Look for Plasmodium parasites.
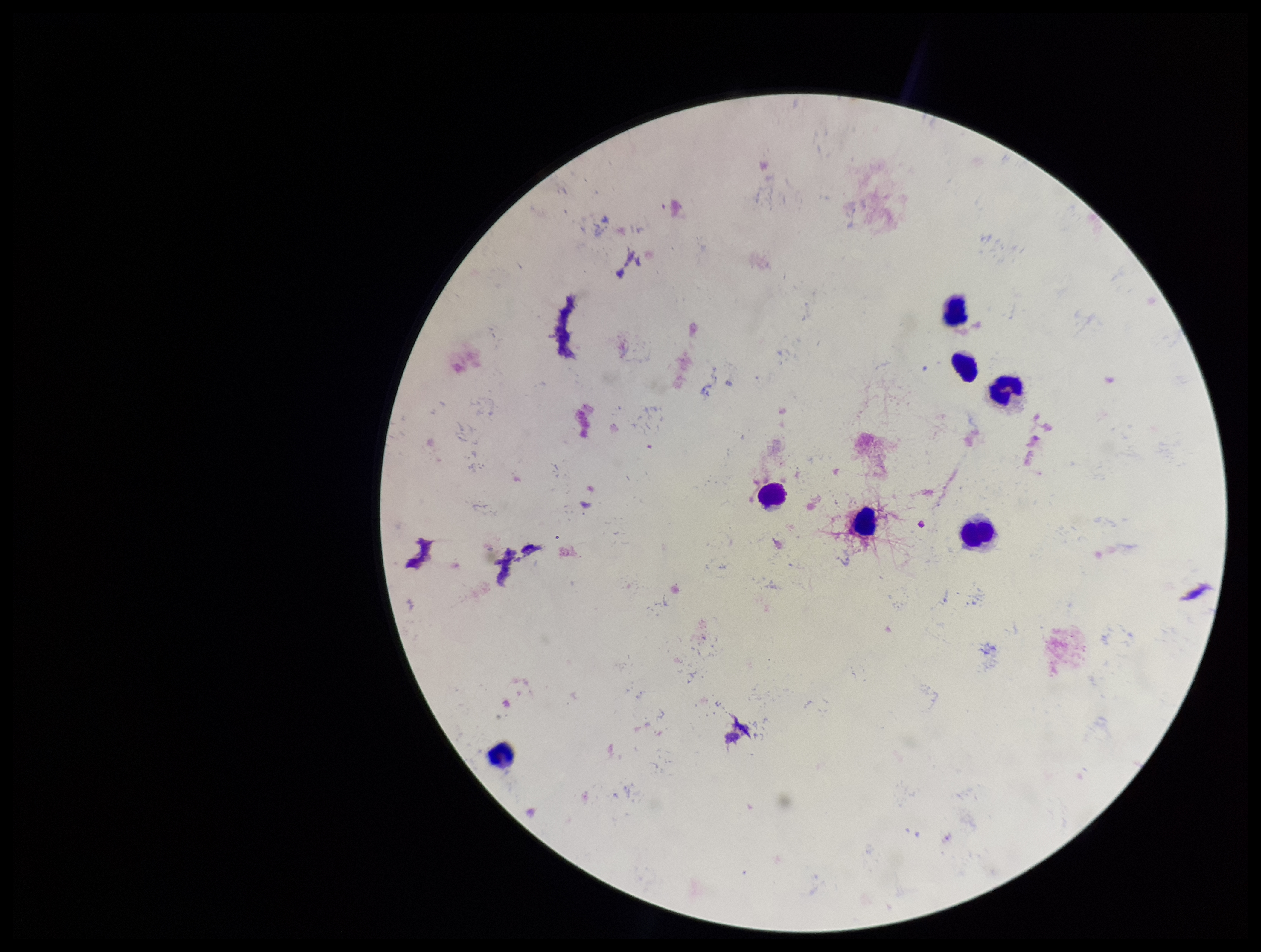
None identified.

Preparation: thick smear. Giemsa stain. Patient malaria status: negative. One field from this slide. Parasite count: 0. Image is 1261×952 pixels. Leukocyte count: 7. Smartphone photograph taken through the eyepiece of a microscope.